State which parasite is depicted.
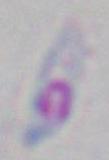
Toxoplasma gondii.

Summary:
  - Modality: photomicrograph
  - Magnification: 1000x